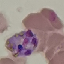
result: malaria parasites identified
preparation: thin blood smear
capture: smartphone camera at the microscope eyepiece
image_type: automatically extracted cell patch, resized to 64 × 64 pixels
stain: Giemsa